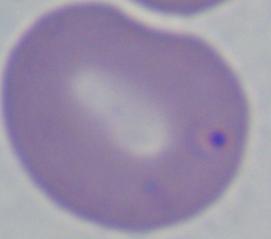

identification = Babesia
modality = photomicrograph
magnification = 1000x